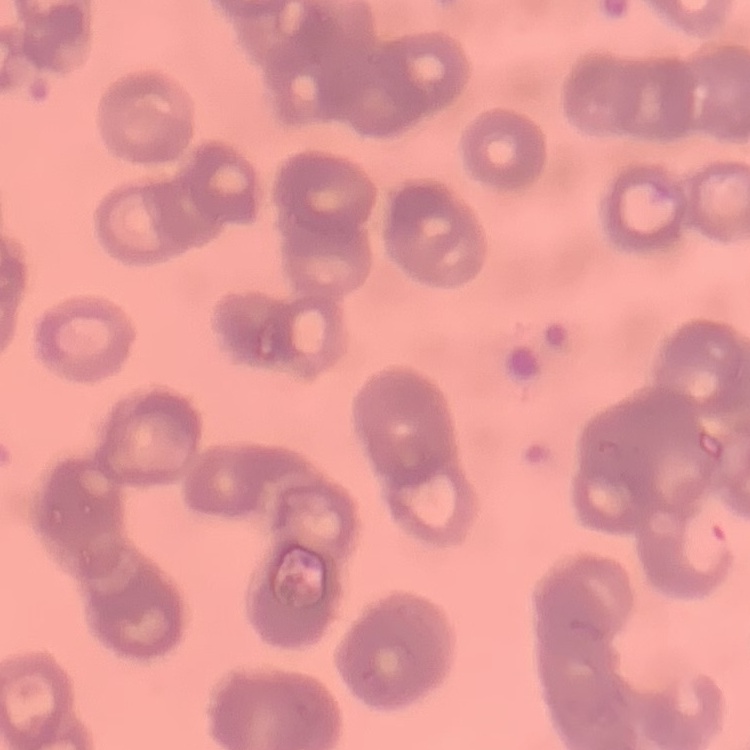
Summary:
  - Erythrocyte morphology: rouleaux formation
  - Stain: Field's or Giemsa
  - Image type: one tile cut from a larger photomicrograph
  - Preparation: thin blood film